Identify the parasite.
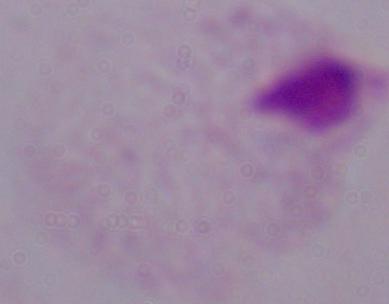
This is a trichomonad.

Summary:
  - Magnification: 1000x
  - Modality: photomicrograph